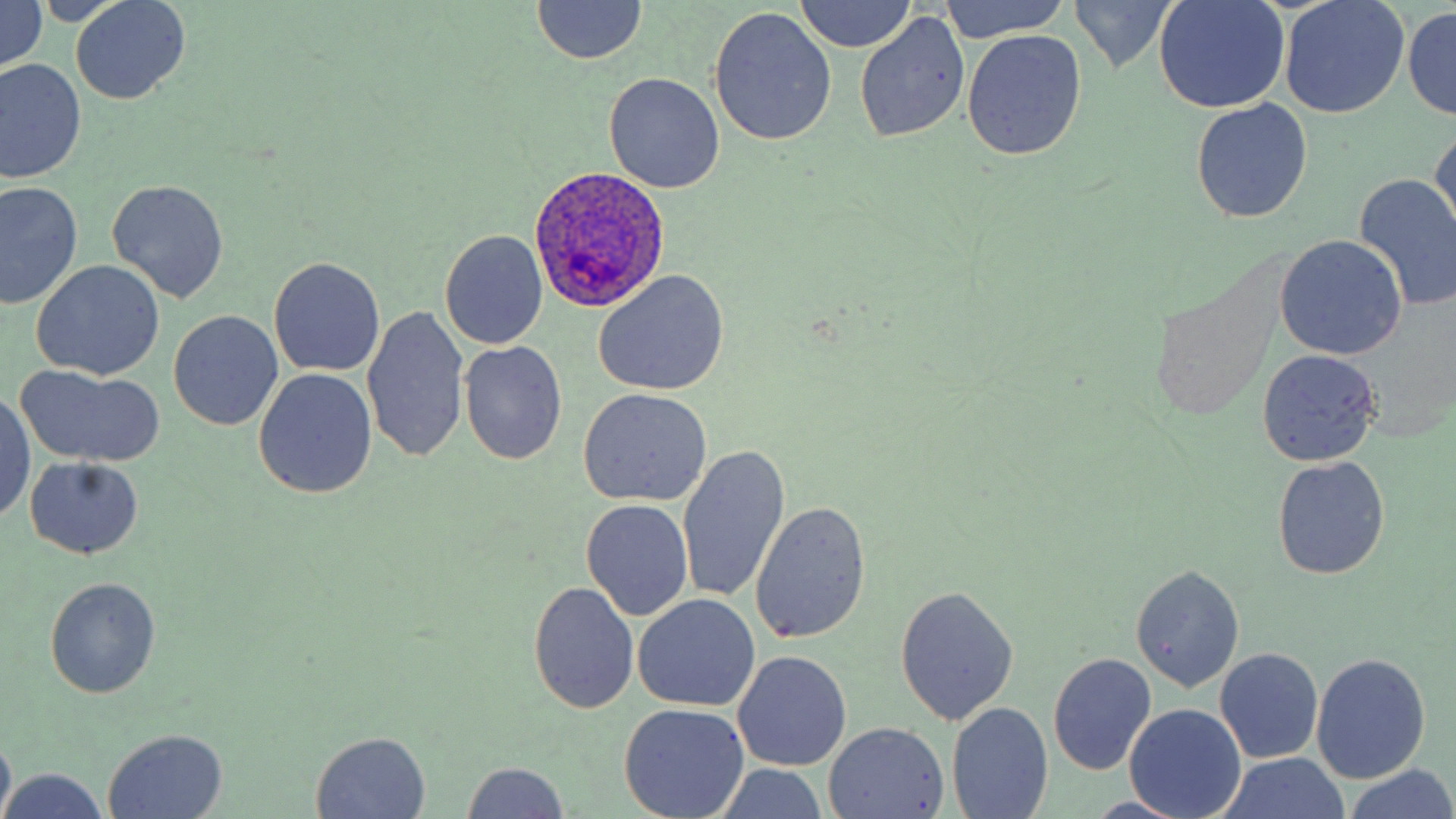

slide-level diagnosis = Plasmodium ovale
preparation = thin blood smear
uninfected red blood cell locations = approximate bounding boxes as (x1,y1)-(x2,y2) corner pairs in pixels: (0,0)-(48,79), (940,0)-(1071,44), (1068,0)-(1182,72), (1156,0)-(1290,114), (1279,0)-(1408,119), (71,1)-(190,105), (532,1)-(647,65), (796,1)-(915,55), (709,7)-(837,146), (1404,8)-(1455,119), (855,13)-(969,142), (963,30)-(1085,160), (1,58)-(85,183), (604,72)-(726,192), (1192,100)-(1312,222), (1430,125)-(1456,239), (1355,173)-(1456,305), (108,179)-(229,303), (1,181)-(80,310), (1309,206)-(1456,339), (440,230)-(548,350), (1274,235)-(1407,360), (270,257)-(385,378), (32,260)-(165,381), (593,270)-(730,397), (362,305)-(470,462), (168,310)-(283,432), (459,341)-(567,466), (1256,350)-(1381,466), (15,368)-(163,468), (253,368)-(377,499), (578,390)-(712,507), (1,393)-(37,524), (677,445)-(790,607), (23,456)-(144,560), (1273,457)-(1390,580), (581,498)-(694,621), (753,500)-(872,645), (1131,563)-(1243,692), (45,578)-(160,698), (528,582)-(640,712), (894,585)-(1018,727), (633,594)-(759,714), (1215,648)-(1324,763), (732,650)-(851,771), (1047,653)-(1157,776), (1312,654)-(1430,784), (619,702)-(749,818), (949,703)-(1053,819), (1126,703)-(1247,819), (824,722)-(951,817), (0,729)-(15,819), (102,729)-(229,818), (310,731)-(432,819), (1217,754)-(1354,819), (459,762)-(571,818), (1343,765)-(1456,819), (3,768)-(110,819)
stain = May-Grünwald-Giemsa
image size = 1456×819 pixels
modality = light microscopy
Plasmodium ovale-infected red blood cell locations = approximate bounding boxes as (x1,y1)-(x2,y2) corner pairs in pixels: (529,164)-(671,311)
field of view = one of a larger specimen
magnification = 1000x